Name the parasite shown.
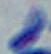
This is Toxoplasma gondii.

1000x magnification. Photomicrograph.